Assess the morphology of the red blood cells.
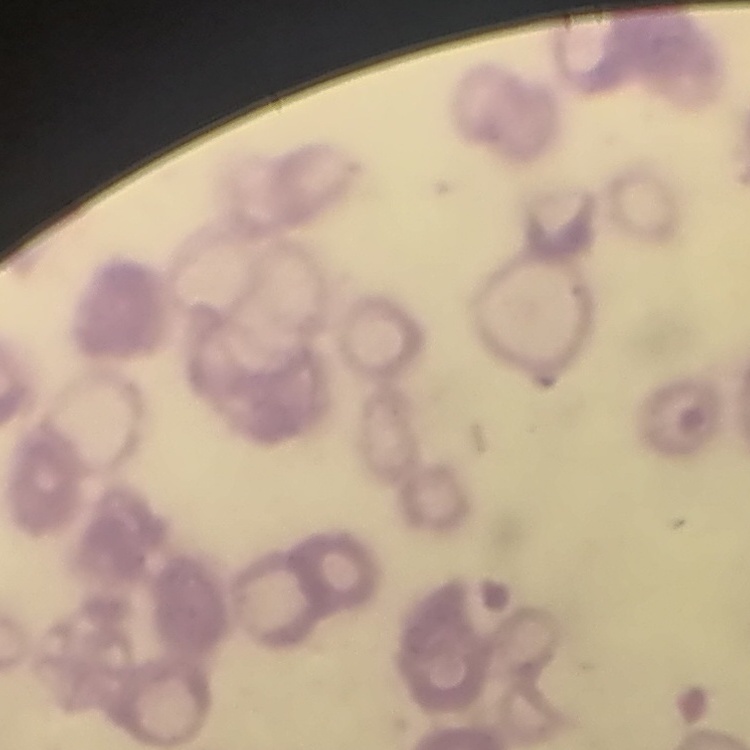
Rouleaux formation.

Thin blood smear. Square crop of a larger photomicrograph. Field's or Giemsa stain.